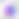
Captured at 400x magnification. Toxoplasma gondii is seen. Micrograph.